Locate every malaria parasite and every leukocyte.
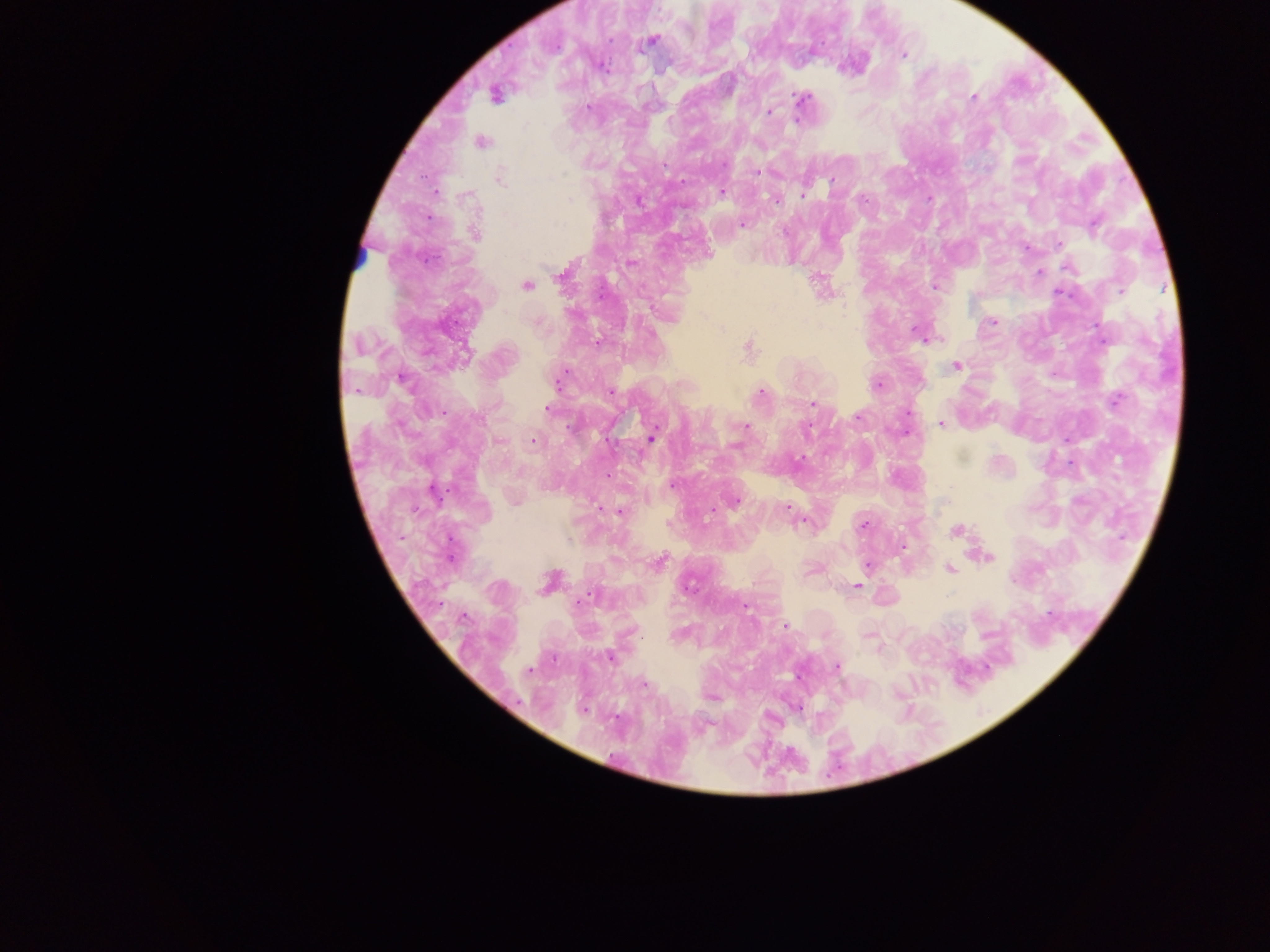

Approximate centers as x y in pixels.
Malaria parasites: 651 40; 903 55; 494 96; 973 97; 800 98; 769 112; 482 142; 665 166; 757 173; 501 179; 832 180; 722 192; 803 193; 570 199; 776 201; 743 224; 475 234; 1059 243; 631 263; 1068 269; 1039 273; 560 275; 526 286; 935 286; 1121 292; 992 322; 921 337; 749 347; 466 353; 956 366; 402 380; 557 382; 877 385; 611 392; 761 392; 1116 400; 812 404; 548 410; 858 417; 941 423; 745 427; 651 437; 533 443; 736 445; 672 485; 735 501; 786 508; 619 512; 863 525; 956 531; 989 557; 659 563; 868 565; 949 569; 688 586; 856 586; 588 597; 746 607; 785 626; 610 657; 837 667; 528 671; 644 684; 583 709.
No leukocytes observed.

Summary:
  - Preparation: thick blood smear
  - Field of view: single
  - Capture: mobile-phone photograph through a microscope
  - Image size: 1270×952 pixels
  - Country: Ghana